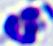
magnification = 400x
modality = photomicrograph
identification = leukocyte